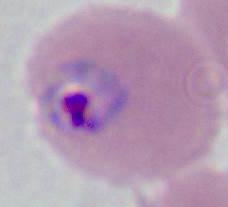 A Plasmodium parasite is seen. Photomicrograph. 400x or 1000x magnification.